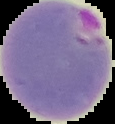
Summary:
  - Malaria status: parasitized
  - Preparation: thin blood smear
  - Image type: segmented cell region with the area outside set to black
  - Image size: 115×124 pixels